Assess for Plasmodium parasites.
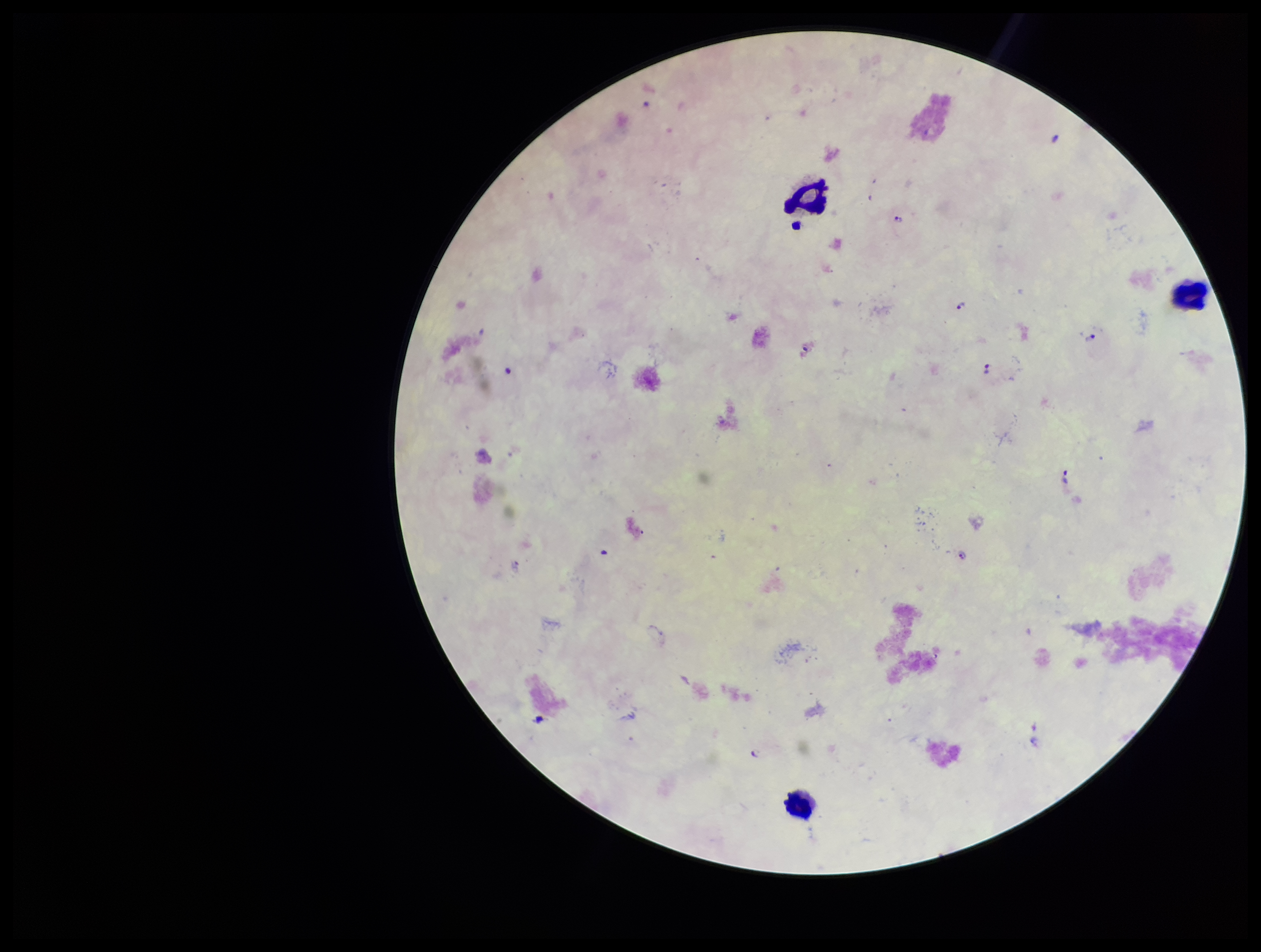
Detected.

Summary:
  - Parasite count: 6
  - Leukocyte count: 3
  - Patient malaria status: infected
  - Stain: Giemsa
  - Preparation: thick
  - Image size: 1261×952 pixels
  - Species reported for this patient: Plasmodium falciparum
  - Capture: smartphone photograph through the microscope eyepiece
  - Field of view: one from this slide